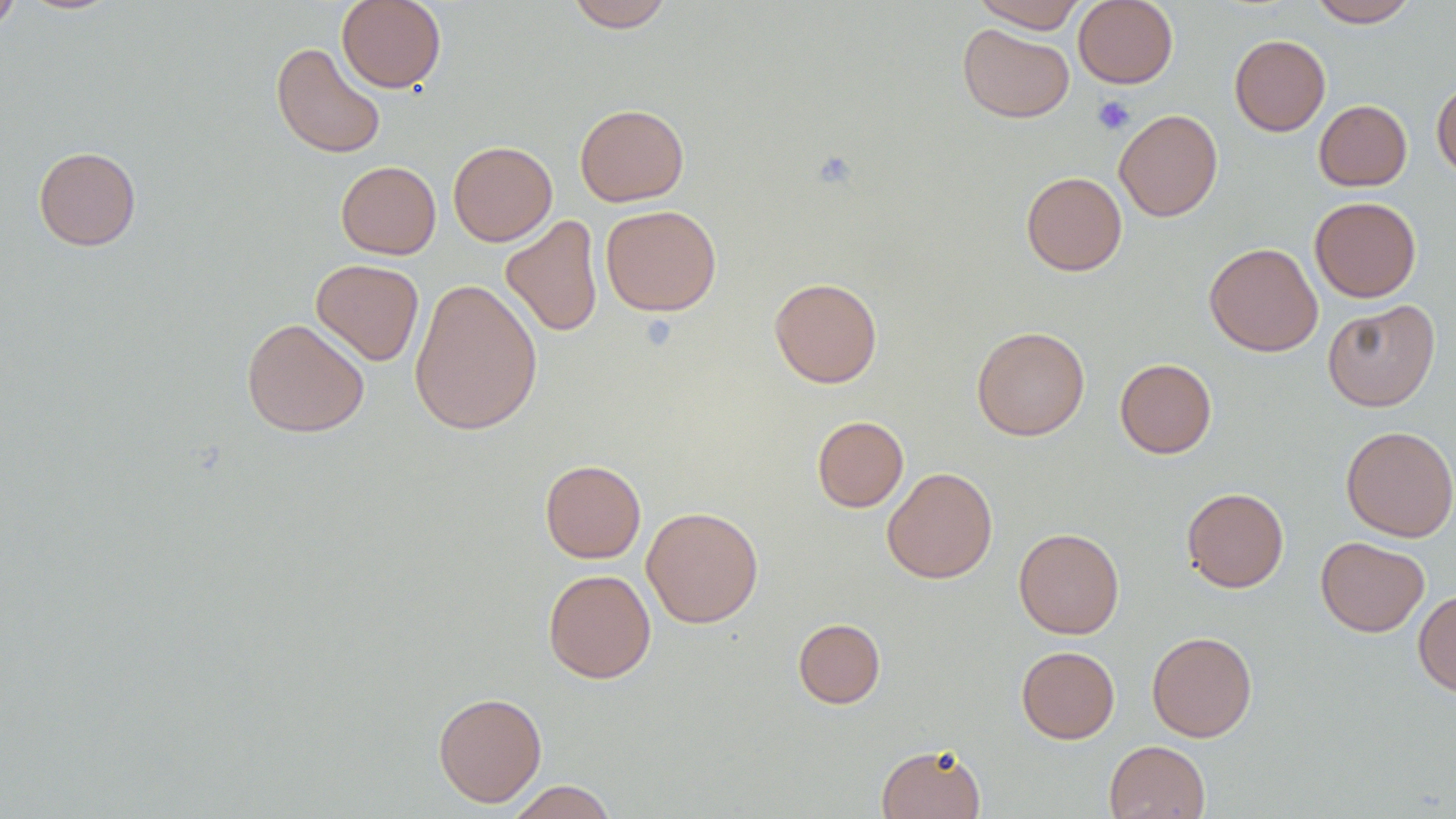
Approximate bounding boxes as named x1/y1/x2/y2 corners in pixels. Uninfected red blood cell locations: (x1=0, y1=0, x2=21, y2=34), (x1=336, y1=0, x2=446, y2=93), (x1=565, y1=0, x2=675, y2=32), (x1=972, y1=0, x2=1087, y2=32), (x1=1073, y1=0, x2=1178, y2=88), (x1=1308, y1=0, x2=1419, y2=27), (x1=957, y1=24, x2=1074, y2=123), (x1=1229, y1=34, x2=1330, y2=136), (x1=271, y1=42, x2=386, y2=159), (x1=1431, y1=79, x2=1456, y2=179), (x1=1313, y1=99, x2=1412, y2=191), (x1=574, y1=103, x2=689, y2=206), (x1=1114, y1=109, x2=1223, y2=222), (x1=448, y1=141, x2=557, y2=246), (x1=33, y1=146, x2=141, y2=250), (x1=335, y1=161, x2=441, y2=259), (x1=1021, y1=171, x2=1127, y2=276), (x1=1309, y1=196, x2=1422, y2=302), (x1=600, y1=204, x2=722, y2=316), (x1=501, y1=215, x2=603, y2=337), (x1=1204, y1=242, x2=1323, y2=357), (x1=311, y1=258, x2=424, y2=366), (x1=769, y1=277, x2=882, y2=388), (x1=409, y1=278, x2=543, y2=436), (x1=1322, y1=299, x2=1440, y2=411), (x1=241, y1=318, x2=369, y2=438), (x1=971, y1=325, x2=1090, y2=441), (x1=1115, y1=358, x2=1217, y2=458), (x1=812, y1=415, x2=909, y2=512), (x1=1340, y1=425, x2=1456, y2=542), (x1=540, y1=460, x2=646, y2=563), (x1=882, y1=466, x2=997, y2=584), (x1=1181, y1=487, x2=1289, y2=593), (x1=641, y1=506, x2=764, y2=628), (x1=1013, y1=527, x2=1124, y2=639), (x1=1316, y1=536, x2=1430, y2=637), (x1=543, y1=569, x2=656, y2=683), (x1=1413, y1=590, x2=1456, y2=698), (x1=792, y1=617, x2=885, y2=708), (x1=1146, y1=631, x2=1257, y2=742), (x1=1016, y1=645, x2=1120, y2=744), (x1=433, y1=691, x2=547, y2=807), (x1=1104, y1=740, x2=1210, y2=819), (x1=876, y1=743, x2=986, y2=818), (x1=505, y1=780, x2=618, y2=819). Platelet locations: (x1=1092, y1=95, x2=1135, y2=136). Slide-level diagnosis: negative for blood parasites. One field of a larger specimen. Captured at 1000x magnification. Image is 1456×819 pixels. Light microscopy. Thin blood smear.